State which parasite is depicted.
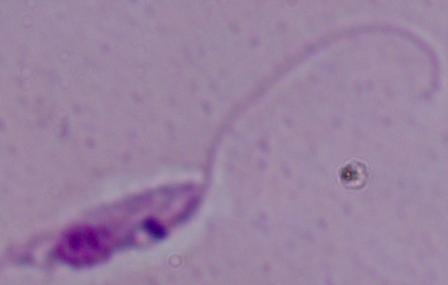
This is Leishmania.

Summary:
  - Magnification: 1000x
  - Modality: photomicrograph